Give the position of every leukocyte visible.
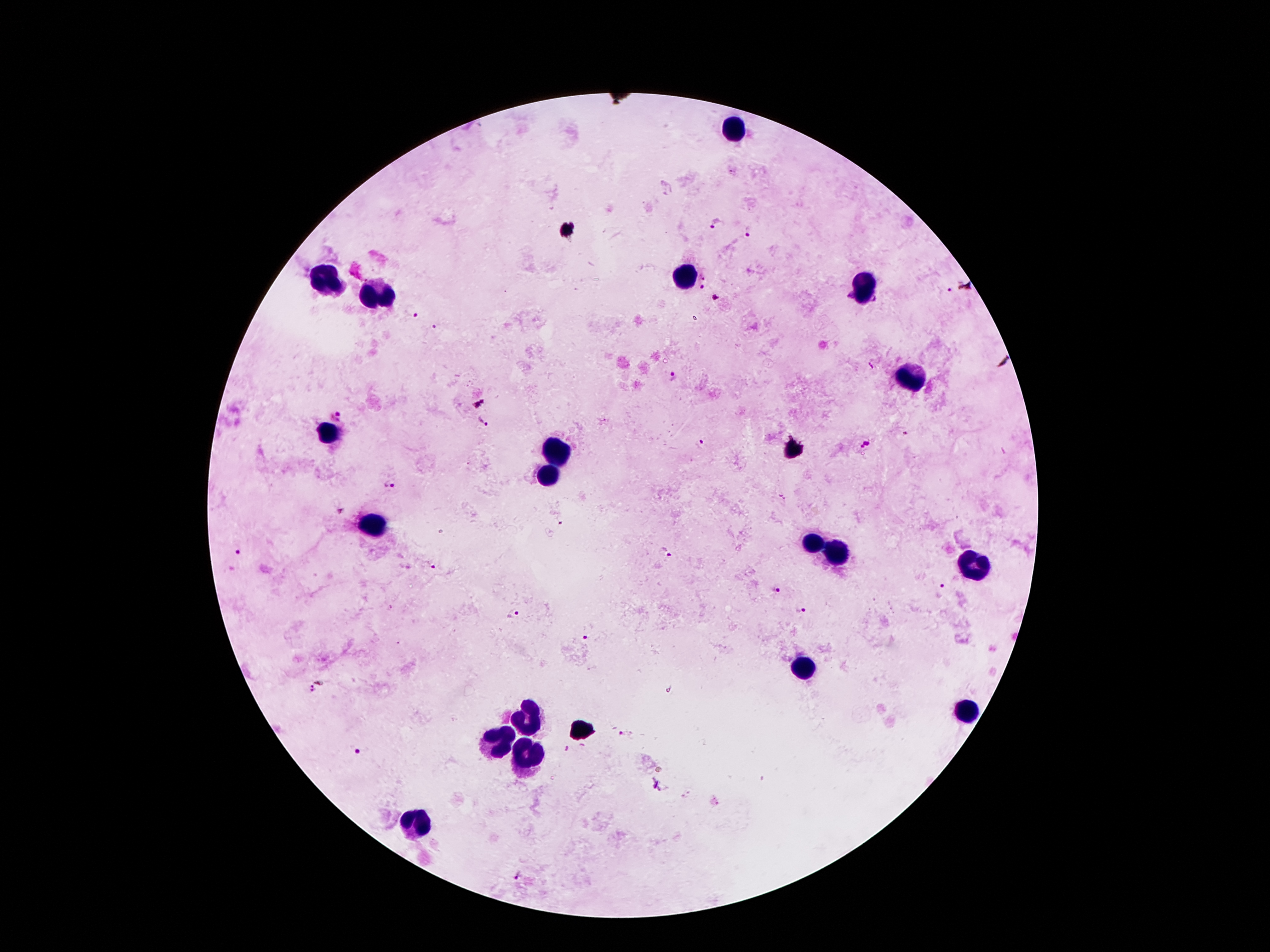
Approximate centers as {x, y} in pixels.
Leukocytes: {735, 130}, {686, 272}, {327, 282}, {865, 288}, {377, 298}, {910, 382}, {332, 434}, {558, 455}, {547, 473}, {370, 527}, {813, 545}, {836, 554}, {974, 563}, {804, 670}, {963, 711}, {529, 718}, {497, 743}, {525, 759}, {416, 825}.

Summary:
  - Malaria parasite locations: {717, 223}, {749, 233}, {703, 286}, {950, 290}, {412, 312}, {434, 327}, {673, 377}, {336, 415}, {484, 421}, {701, 445}, {865, 445}, {389, 483}, {667, 551}, {237, 553}, {432, 568}, {775, 587}, {942, 590}, {802, 613}, {515, 614}, {583, 636}, {323, 680}, {307, 691}, {359, 751}, {658, 786}, {517, 876}
  - Preparation: thick peripheral-blood smear
  - Magnification: 100x
  - Image size: 1270×952 pixels
  - Stain: Giemsa
  - Patient malaria status: positive for Plasmodium falciparum
  - Field of view: one from this slide
  - Capture: smartphone camera through the microscope eyepiece